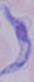
modality = micrograph
identification = trypanosome
magnification = 1000x